Identify the parasite.
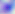

This is Toxoplasma gondii.

Summary:
  - Modality: micrograph
  - Magnification: 400x